Give the extent of all uninfected red blood cells.
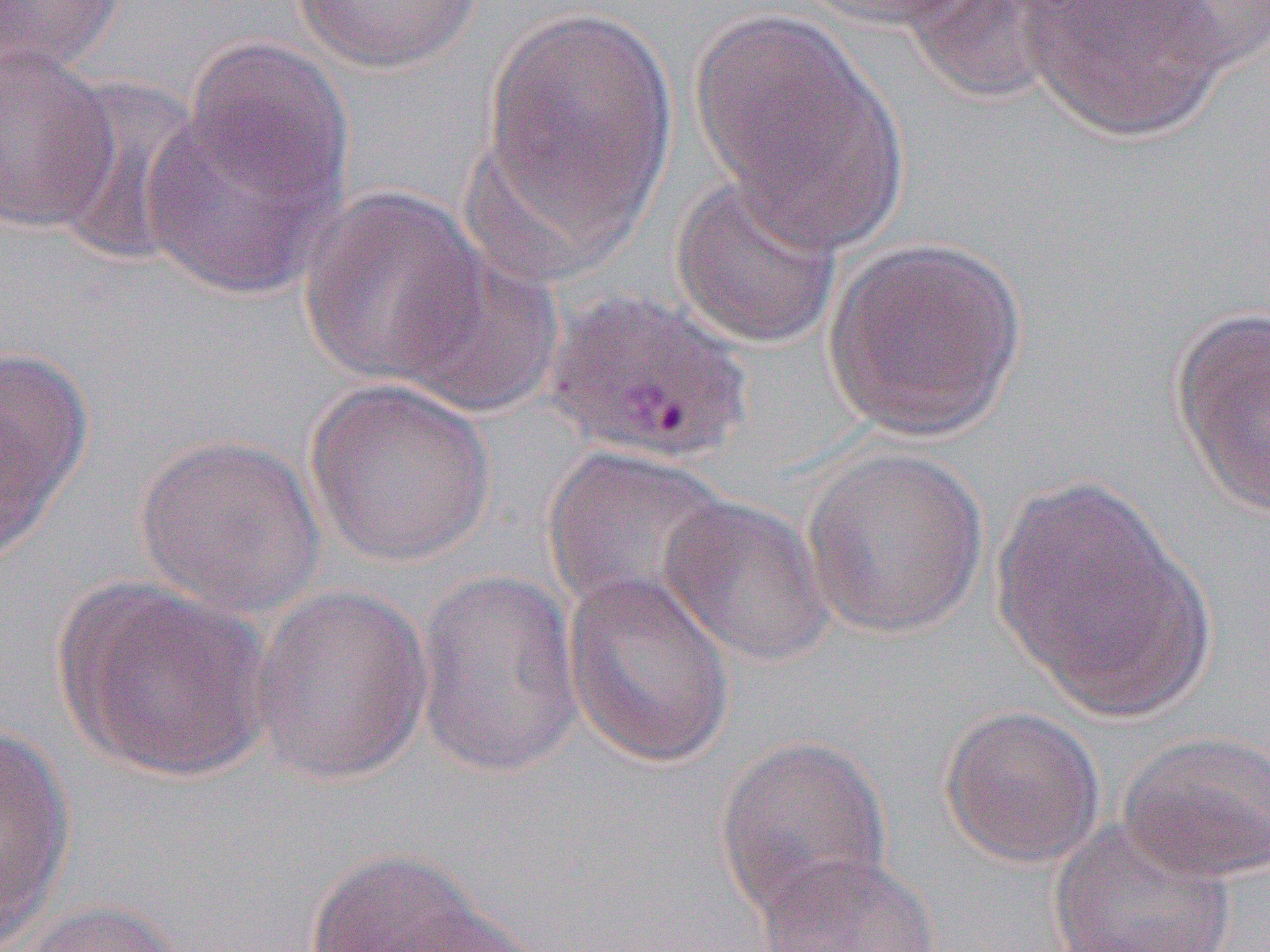
Approximate bounding boxes as [x1, y1, x2, y2] in pixels.
Uninfected red blood cells: [0, 0, 128, 77], [289, 0, 489, 74], [796, 0, 985, 32], [905, 0, 1060, 108], [1012, 0, 1235, 141], [1127, 1, 1270, 75], [478, 5, 679, 256], [689, 11, 909, 251], [184, 37, 354, 208], [0, 45, 118, 234], [45, 73, 209, 266], [139, 97, 347, 300], [668, 172, 846, 352], [298, 185, 491, 387], [821, 236, 1030, 443], [394, 250, 563, 417], [1170, 307, 1270, 519], [0, 349, 93, 553], [303, 378, 497, 568], [133, 432, 327, 618], [540, 446, 735, 623], [801, 446, 991, 639], [991, 474, 1215, 720], [659, 495, 835, 668], [561, 566, 736, 769], [413, 569, 585, 780], [54, 577, 274, 784], [248, 584, 434, 787], [939, 706, 1106, 869], [0, 726, 74, 944], [1116, 731, 1270, 885], [714, 734, 893, 921], [1047, 816, 1238, 952], [303, 846, 512, 952], [754, 852, 944, 952], [9, 900, 187, 952], [384, 903, 551, 951].

Summary:
  - Slide-level diagnosis: Plasmodium vivax
  - Magnification: 1000x
  - Preparation: thin blood film
  - Field of view: one of a larger specimen
  - Modality: light microscopy
  - Image size: 1270×952 pixels